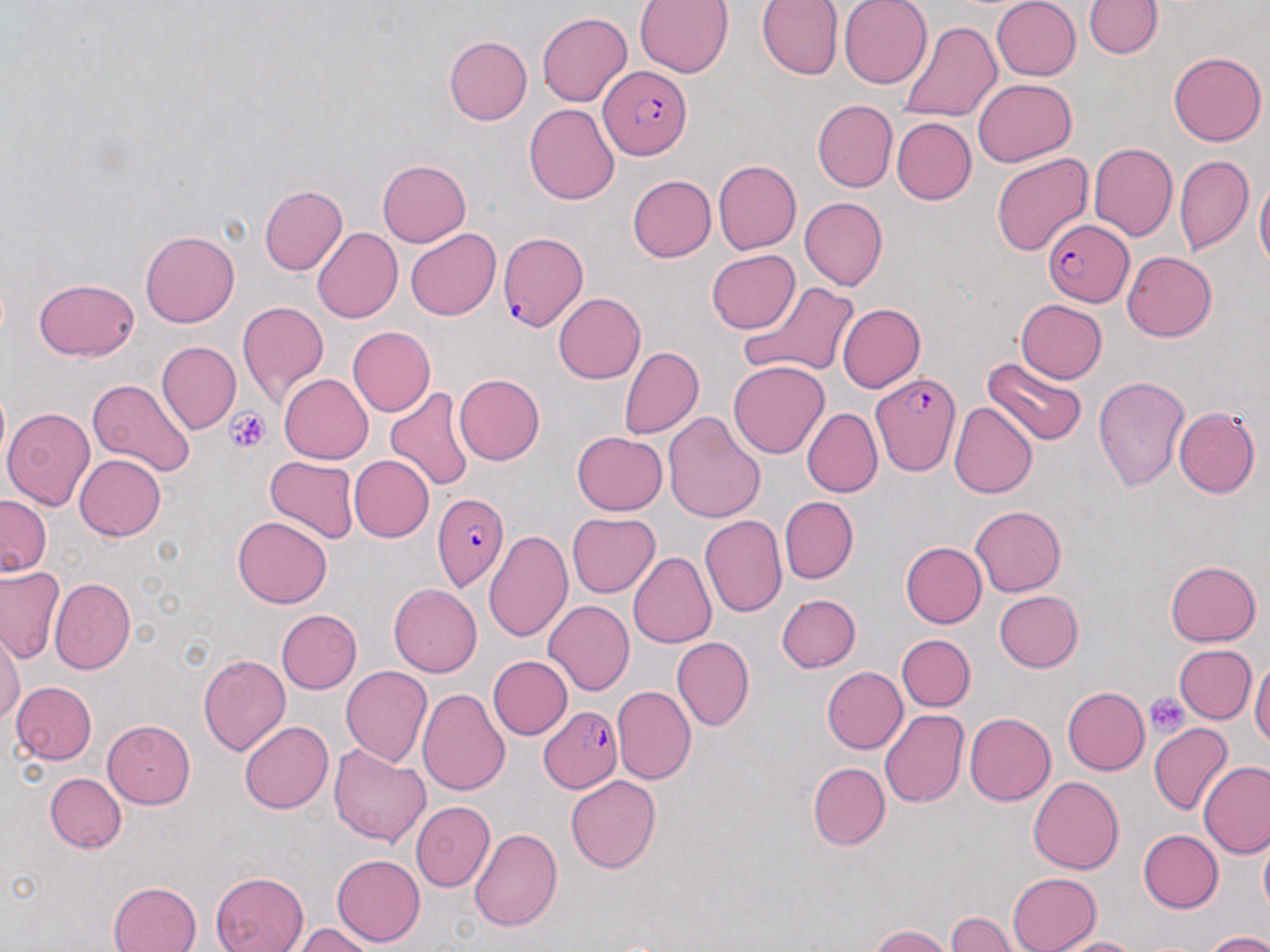

Summary:
  - Coordinate format: approximate bounding boxes as named x1/y1/x2/y2 corners in pixels
  - Platelet locations: (x1=225, y1=409, x2=272, y2=455), (x1=1145, y1=693, x2=1188, y2=740)
  - Plasmodium falciparum-infected red blood cell locations: (x1=597, y1=66, x2=693, y2=161), (x1=1042, y1=219, x2=1132, y2=307), (x1=499, y1=232, x2=589, y2=333), (x1=870, y1=372, x2=963, y2=476), (x1=433, y1=493, x2=510, y2=592), (x1=537, y1=706, x2=622, y2=794)
  - Uninfected red blood cell locations: (x1=634, y1=0, x2=733, y2=78), (x1=756, y1=0, x2=843, y2=80), (x1=837, y1=0, x2=932, y2=88), (x1=991, y1=0, x2=1082, y2=80), (x1=1086, y1=0, x2=1160, y2=60), (x1=538, y1=12, x2=632, y2=106), (x1=898, y1=18, x2=1005, y2=124), (x1=443, y1=36, x2=529, y2=124), (x1=1168, y1=50, x2=1265, y2=145), (x1=972, y1=78, x2=1074, y2=167), (x1=812, y1=100, x2=897, y2=192), (x1=524, y1=103, x2=618, y2=205), (x1=891, y1=118, x2=975, y2=205), (x1=1089, y1=142, x2=1177, y2=240), (x1=1175, y1=152, x2=1254, y2=255), (x1=991, y1=153, x2=1093, y2=256), (x1=375, y1=160, x2=470, y2=247), (x1=711, y1=160, x2=801, y2=255), (x1=626, y1=175, x2=716, y2=263), (x1=1254, y1=177, x2=1269, y2=281), (x1=261, y1=183, x2=347, y2=276), (x1=801, y1=198, x2=888, y2=290), (x1=310, y1=227, x2=402, y2=323), (x1=140, y1=229, x2=239, y2=327), (x1=406, y1=230, x2=501, y2=320), (x1=706, y1=249, x2=800, y2=334), (x1=1121, y1=250, x2=1217, y2=342), (x1=33, y1=278, x2=140, y2=361), (x1=736, y1=279, x2=861, y2=381), (x1=554, y1=293, x2=645, y2=384), (x1=1012, y1=299, x2=1107, y2=385), (x1=235, y1=300, x2=328, y2=407), (x1=836, y1=302, x2=924, y2=391), (x1=346, y1=326, x2=434, y2=416), (x1=157, y1=341, x2=240, y2=432), (x1=618, y1=345, x2=703, y2=441), (x1=983, y1=355, x2=1086, y2=448), (x1=729, y1=359, x2=829, y2=461), (x1=453, y1=373, x2=545, y2=465), (x1=278, y1=374, x2=373, y2=464), (x1=1093, y1=375, x2=1193, y2=492), (x1=87, y1=379, x2=197, y2=479), (x1=384, y1=386, x2=475, y2=493), (x1=948, y1=402, x2=1037, y2=500), (x1=3, y1=405, x2=98, y2=510), (x1=804, y1=407, x2=883, y2=497), (x1=1174, y1=407, x2=1259, y2=498), (x1=662, y1=411, x2=765, y2=524), (x1=572, y1=431, x2=668, y2=516), (x1=74, y1=452, x2=167, y2=539), (x1=348, y1=455, x2=431, y2=541), (x1=265, y1=457, x2=356, y2=547), (x1=778, y1=495, x2=858, y2=582), (x1=0, y1=496, x2=49, y2=579), (x1=969, y1=505, x2=1067, y2=596), (x1=566, y1=511, x2=659, y2=598), (x1=700, y1=516, x2=786, y2=618), (x1=232, y1=517, x2=331, y2=608), (x1=487, y1=528, x2=574, y2=644), (x1=900, y1=540, x2=986, y2=627), (x1=629, y1=552, x2=715, y2=649), (x1=1166, y1=559, x2=1262, y2=648), (x1=1, y1=566, x2=65, y2=663), (x1=50, y1=577, x2=135, y2=675), (x1=388, y1=584, x2=481, y2=677), (x1=993, y1=589, x2=1083, y2=673), (x1=775, y1=591, x2=860, y2=671), (x1=544, y1=601, x2=634, y2=694), (x1=278, y1=609, x2=361, y2=693), (x1=896, y1=635, x2=974, y2=711), (x1=0, y1=636, x2=23, y2=727), (x1=672, y1=637, x2=753, y2=731), (x1=1173, y1=644, x2=1255, y2=725), (x1=198, y1=652, x2=290, y2=755), (x1=487, y1=654, x2=572, y2=739), (x1=1251, y1=659, x2=1269, y2=759), (x1=340, y1=662, x2=433, y2=767), (x1=820, y1=666, x2=907, y2=755), (x1=10, y1=681, x2=97, y2=766), (x1=418, y1=686, x2=510, y2=797), (x1=613, y1=686, x2=696, y2=785), (x1=1060, y1=686, x2=1147, y2=776), (x1=880, y1=708, x2=968, y2=808), (x1=963, y1=710, x2=1055, y2=803), (x1=240, y1=719, x2=333, y2=814), (x1=102, y1=720, x2=194, y2=808), (x1=1150, y1=722, x2=1231, y2=816), (x1=1159, y1=736, x2=1258, y2=849), (x1=330, y1=744, x2=430, y2=844), (x1=1201, y1=758, x2=1270, y2=857), (x1=807, y1=761, x2=890, y2=851), (x1=45, y1=773, x2=125, y2=853), (x1=566, y1=776, x2=661, y2=874), (x1=1027, y1=776, x2=1123, y2=874), (x1=410, y1=802, x2=494, y2=892), (x1=469, y1=826, x2=562, y2=933), (x1=1137, y1=829, x2=1224, y2=913), (x1=1258, y1=841, x2=1270, y2=921), (x1=331, y1=854, x2=425, y2=946), (x1=211, y1=872, x2=308, y2=952), (x1=1005, y1=872, x2=1102, y2=952), (x1=108, y1=879, x2=203, y2=952), (x1=946, y1=911, x2=1014, y2=952), (x1=294, y1=923, x2=371, y2=952), (x1=870, y1=924, x2=953, y2=952), (x1=1200, y1=930, x2=1270, y2=951), (x1=1057, y1=934, x2=1146, y2=951)
  - Slide-level diagnosis: Plasmodium falciparum
  - Image size: 1270×952 pixels
  - Modality: optical microscopy
  - Preparation: thin blood smear
  - Field of view: single
  - Stain: May-Grünwald-Giemsa
  - Magnification: 1000x